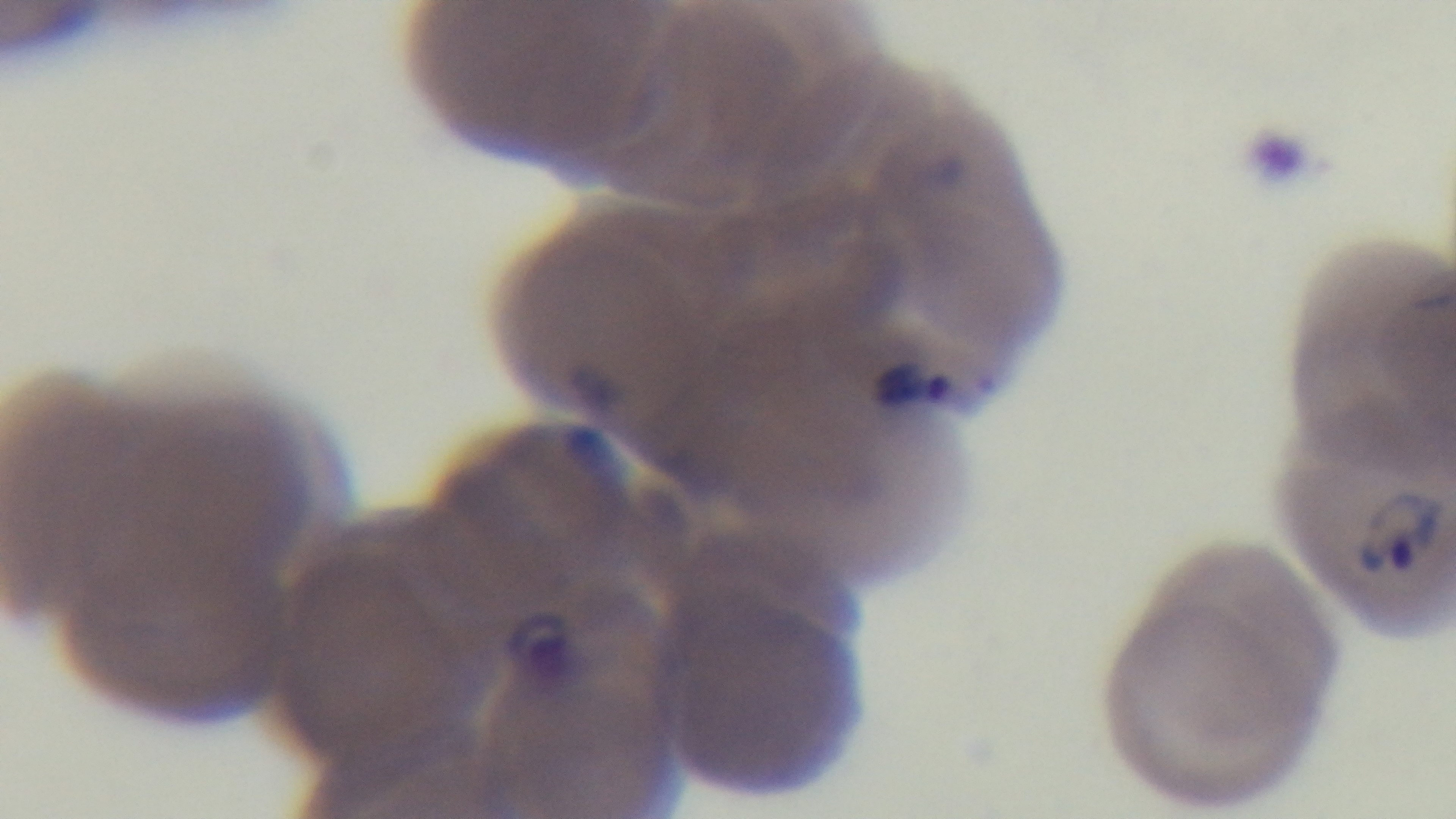

Summary:
  - Preparation: thin blood film
  - Field of view: single
  - Stain: Giemsa
  - Objective: 100x oil immersion
  - Capture: mounted 4K digital camera
  - Modality: light microscopy
  - Malaria status: infected